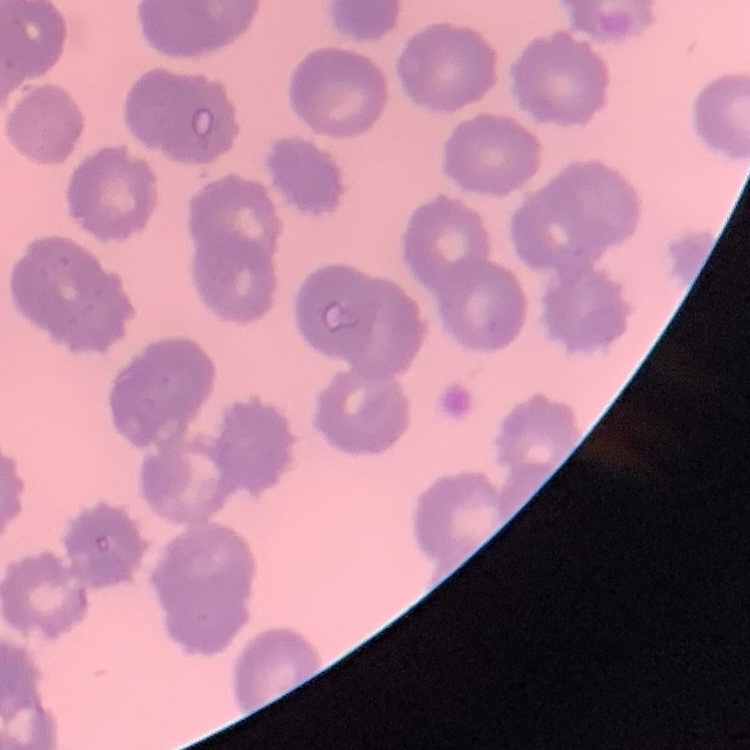

erythrocyte morphology = no rouleaux formation
image type = square crop of a larger photomicrograph
preparation = thin blood film
stain = Field's or Giemsa